Classify this cell by malaria status.
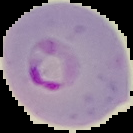
It is parasitized.

Summary:
  - Image size: 133×133 pixels
  - Image type: cell region segmented out of the field of view; surrounding area masked to black
  - Preparation: thin blood smear